Report the malaria status of this cell.
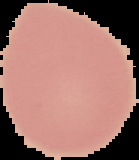
Uninfected.

Image is 139×160 pixels. Segmented cell region on a black background. From a thin blood smear.